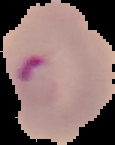
Summary:
  - Image size: 115×145 pixels
  - Preparation: thin blood film
  - Image type: cell region segmented out of the field of view; surrounding area masked to black
  - Malaria status: parasitized